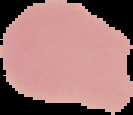
Malaria status: uninfected. The area outside the segmented cell region is set to black. Image is 133×115 pixels. From a thin blood smear.